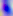

magnification = 400x
modality = photomicrograph
identification = Toxoplasma gondii